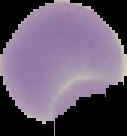 The area outside the segmented cell region is set to black. Result: no Plasmodium parasites seen. Image is 127×136 pixels. From a thin blood film.